Identify the parasite.
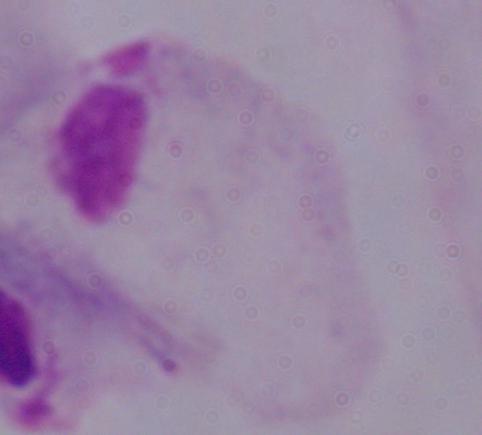
A trichomonad.

1000x magnification. Micrograph.